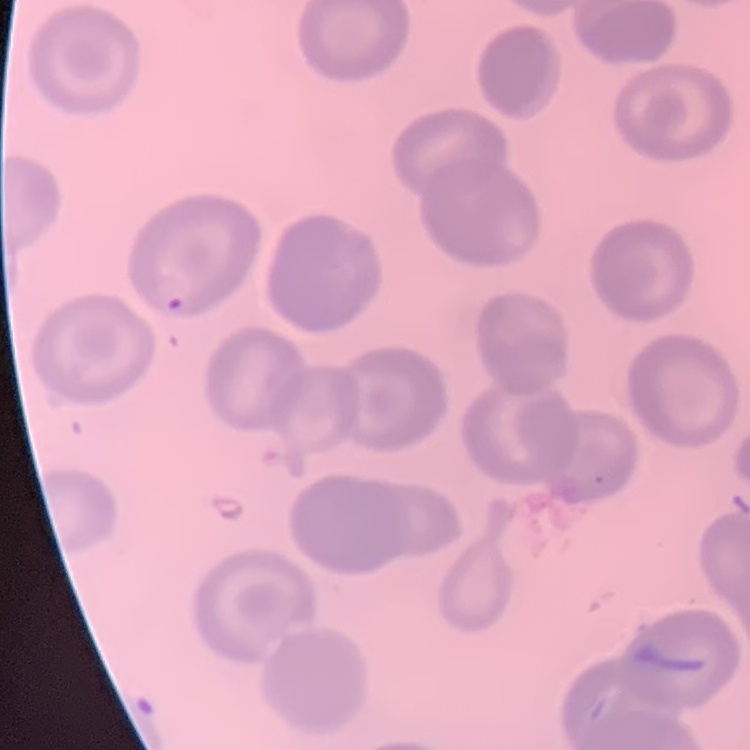

Summary:
  - Erythrocyte morphology: no rouleaux formation
  - Stain: Field's or Giemsa
  - Image type: one tile cut from a larger photomicrograph
  - Preparation: thin blood film